Classify this cell by malaria status.
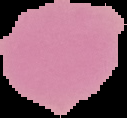
Uninfected.

Image is 127×118 pixels. Segmented cell region on a black background. From a thin blood film.